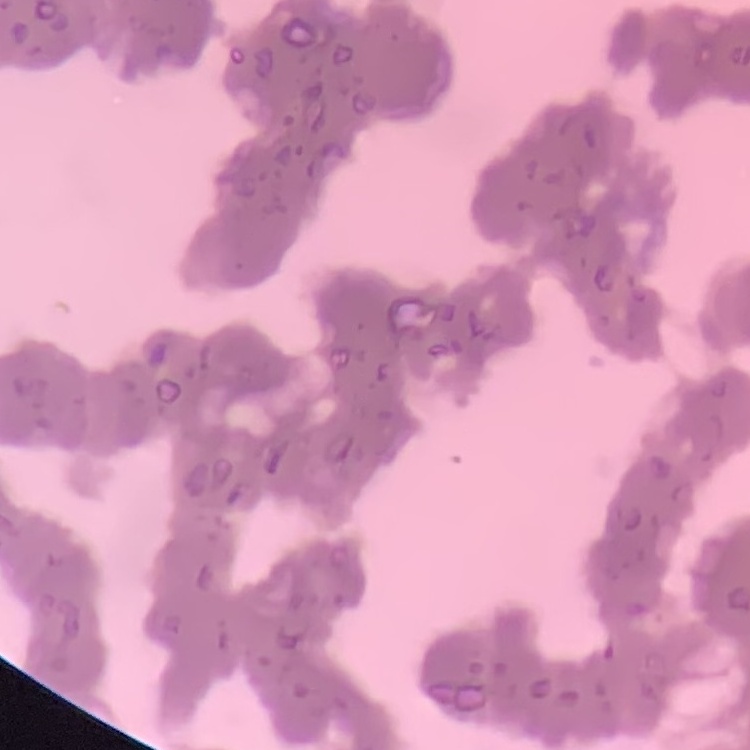
Summary:
  - Erythrocyte morphology: rouleaux formation
  - Preparation: thin peripheral smear
  - Image type: square crop of a larger photomicrograph
  - Stain: Field's or Giemsa